Locate every blood parasite and identify its species.
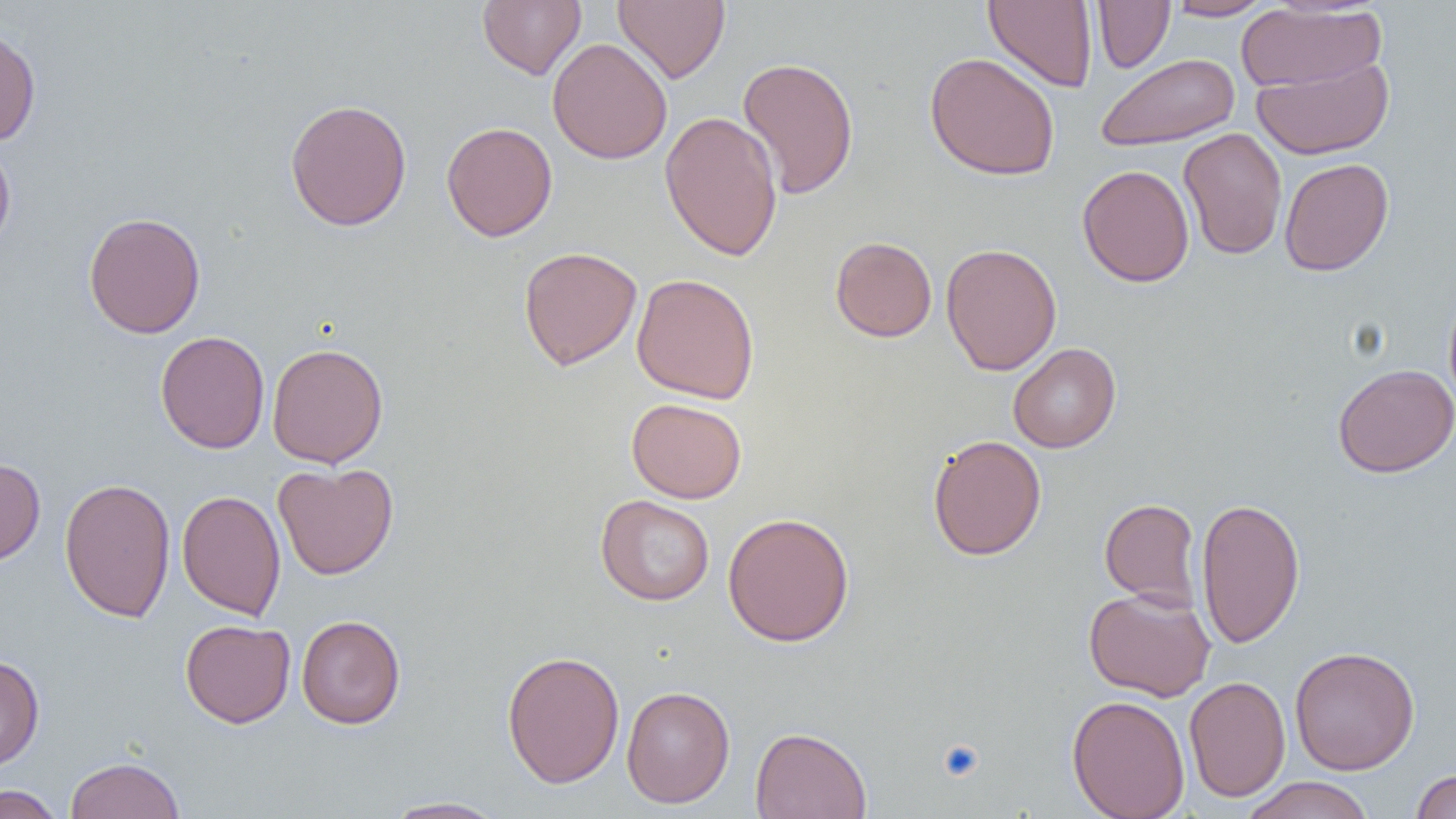
No blood parasites observed.

slide-level diagnosis = no evidence of blood parasites
field of view = one of a larger specimen
modality = optical microscopy
image size = 1456×819 pixels
preparation = thin blood smear
uninfected red blood cell locations = approximate bounding boxes as (x1,y1)-(x2,y2) corner pairs in pixels: (613,0)-(730,84), (1092,0)-(1175,72), (1165,0)-(1276,21), (477,1)-(586,80), (983,1)-(1098,91), (1236,3)-(1386,93), (0,24)-(41,147), (547,37)-(672,164), (924,52)-(1060,181), (1097,53)-(1239,151), (737,56)-(859,200), (1252,56)-(1394,160), (284,98)-(412,231), (660,111)-(784,262), (441,121)-(558,242), (1178,128)-(1288,260), (0,136)-(16,256), (1279,158)-(1394,277), (1077,164)-(1195,288), (83,211)-(206,339), (830,236)-(937,342), (940,242)-(1062,375), (518,246)-(642,371), (632,273)-(760,404), (1443,285)-(1456,412), (154,330)-(270,454), (267,342)-(389,468), (1008,343)-(1121,453), (1332,364)-(1456,478), (626,398)-(747,503), (928,434)-(1046,561), (0,457)-(46,567), (272,462)-(399,580), (59,477)-(176,622), (177,490)-(286,620), (595,494)-(715,606), (1195,495)-(1305,649), (1099,497)-(1202,610), (722,512)-(855,646), (1084,587)-(1215,701), (296,614)-(406,729), (180,619)-(295,728), (1289,646)-(1420,775), (501,650)-(625,789), (0,654)-(44,771), (1184,675)-(1291,802), (621,685)-(735,808), (1066,694)-(1190,819), (750,726)-(872,819), (65,756)-(184,819), (1410,769)-(1456,819), (1240,776)-(1376,819), (0,784)-(66,819), (380,796)-(509,818)
platelet locations = approximate bounding boxes as (x1,y1)-(x2,y2) corner pairs in pixels: (940,739)-(985,783)
magnification = 1000x